Assess this cell for malaria.
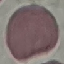
It is uninfected.

Summary:
  - Stain: Giemsa
  - Capture: smartphone through the microscope eyepiece
  - Image type: cell patch, automatically extracted from a larger field of view and resized to 64 × 64 pixels
  - Preparation: thin smear